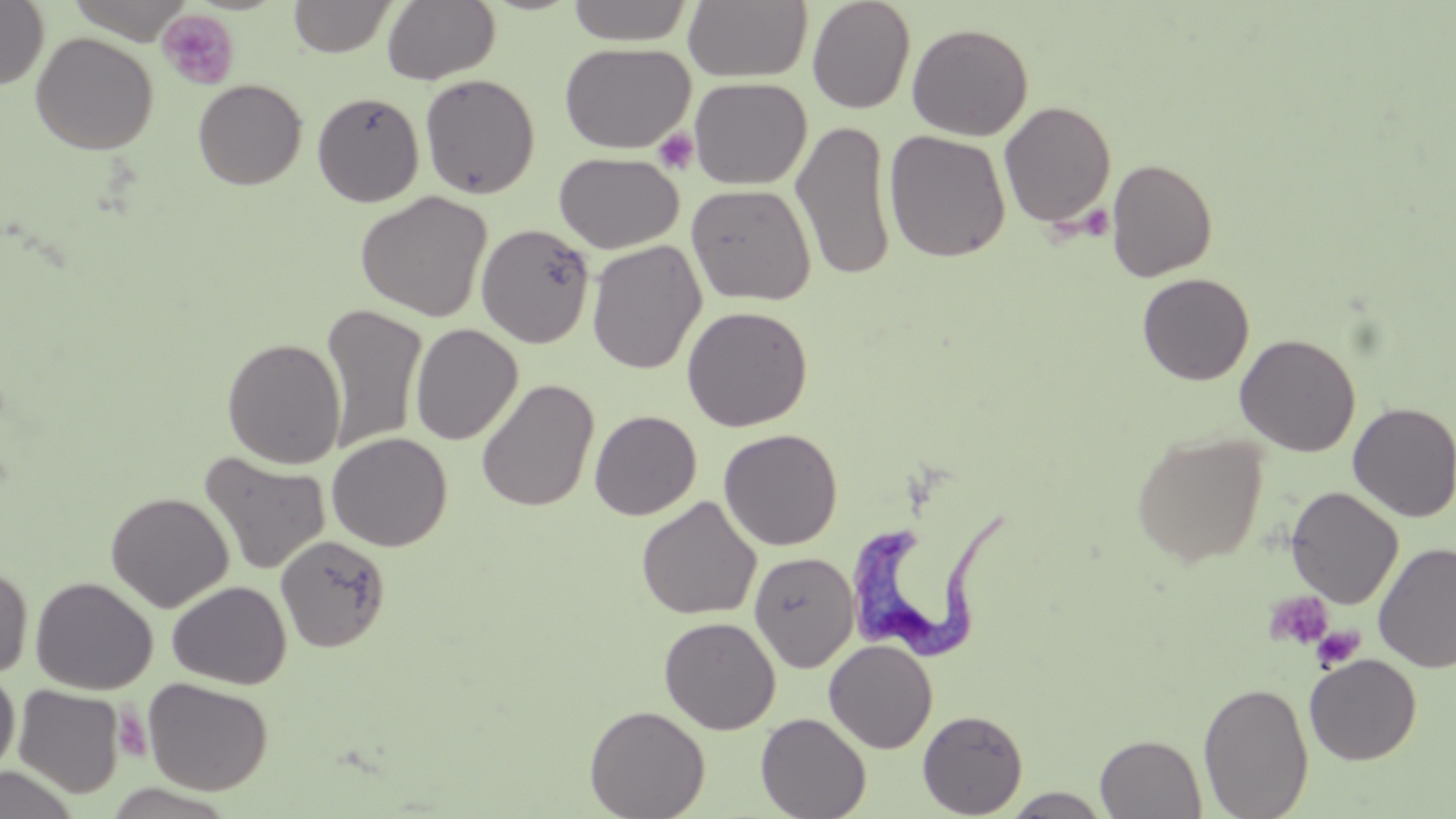

Approximate bounding boxes as named x1/y1/x2/y2 corners in pixels. Uninfected red blood cell locations: (x1=66, y1=0, x2=193, y2=43), (x1=288, y1=0, x2=398, y2=58), (x1=381, y1=0, x2=501, y2=85), (x1=566, y1=0, x2=694, y2=46), (x1=683, y1=0, x2=812, y2=83), (x1=806, y1=0, x2=916, y2=114), (x1=0, y1=1, x2=49, y2=89), (x1=906, y1=23, x2=1033, y2=141), (x1=30, y1=32, x2=158, y2=154), (x1=559, y1=42, x2=694, y2=154), (x1=419, y1=73, x2=541, y2=199), (x1=688, y1=77, x2=811, y2=190), (x1=192, y1=79, x2=307, y2=190), (x1=312, y1=91, x2=425, y2=207), (x1=998, y1=100, x2=1117, y2=229), (x1=791, y1=119, x2=896, y2=282), (x1=883, y1=130, x2=1011, y2=263), (x1=554, y1=152, x2=683, y2=254), (x1=1106, y1=157, x2=1217, y2=282), (x1=686, y1=183, x2=816, y2=306), (x1=355, y1=191, x2=493, y2=322), (x1=476, y1=223, x2=595, y2=348), (x1=587, y1=240, x2=707, y2=375), (x1=1137, y1=273, x2=1255, y2=385), (x1=321, y1=303, x2=428, y2=454), (x1=681, y1=305, x2=813, y2=432), (x1=409, y1=323, x2=523, y2=445), (x1=1235, y1=334, x2=1361, y2=457), (x1=222, y1=337, x2=346, y2=469), (x1=476, y1=378, x2=599, y2=512), (x1=1347, y1=402, x2=1456, y2=522), (x1=589, y1=410, x2=702, y2=520), (x1=718, y1=428, x2=842, y2=551), (x1=326, y1=432, x2=452, y2=552), (x1=1131, y1=432, x2=1267, y2=568), (x1=199, y1=451, x2=331, y2=575), (x1=1285, y1=486, x2=1403, y2=609), (x1=105, y1=491, x2=233, y2=613), (x1=636, y1=496, x2=762, y2=621), (x1=275, y1=535, x2=391, y2=652), (x1=1373, y1=543, x2=1456, y2=672), (x1=749, y1=551, x2=859, y2=672), (x1=0, y1=560, x2=34, y2=680), (x1=30, y1=576, x2=157, y2=695), (x1=167, y1=581, x2=292, y2=690), (x1=659, y1=616, x2=781, y2=734), (x1=823, y1=639, x2=938, y2=754), (x1=1304, y1=654, x2=1422, y2=765), (x1=0, y1=668, x2=20, y2=780), (x1=143, y1=678, x2=273, y2=795), (x1=1198, y1=680, x2=1315, y2=819), (x1=13, y1=684, x2=125, y2=798), (x1=584, y1=704, x2=711, y2=819), (x1=917, y1=709, x2=1028, y2=818), (x1=756, y1=712, x2=871, y2=819), (x1=1095, y1=734, x2=1207, y2=818), (x1=0, y1=766, x2=80, y2=818), (x1=101, y1=784, x2=240, y2=818), (x1=1000, y1=788, x2=1114, y2=818). Platelet locations: (x1=156, y1=9, x2=240, y2=90), (x1=653, y1=128, x2=699, y2=175), (x1=1079, y1=204, x2=1114, y2=240), (x1=1263, y1=590, x2=1334, y2=651), (x1=1310, y1=625, x2=1365, y2=672), (x1=114, y1=708, x2=151, y2=762). Trypanosoma brucei locations: (x1=851, y1=506, x2=1010, y2=660). Slide-level diagnosis: Trypanosoma brucei. Light microscopy. Thin blood smear. Captured at 1000x magnification. May-Grünwald-Giemsa-stained preparation. Single field of view. Image is 1456×819 pixels.